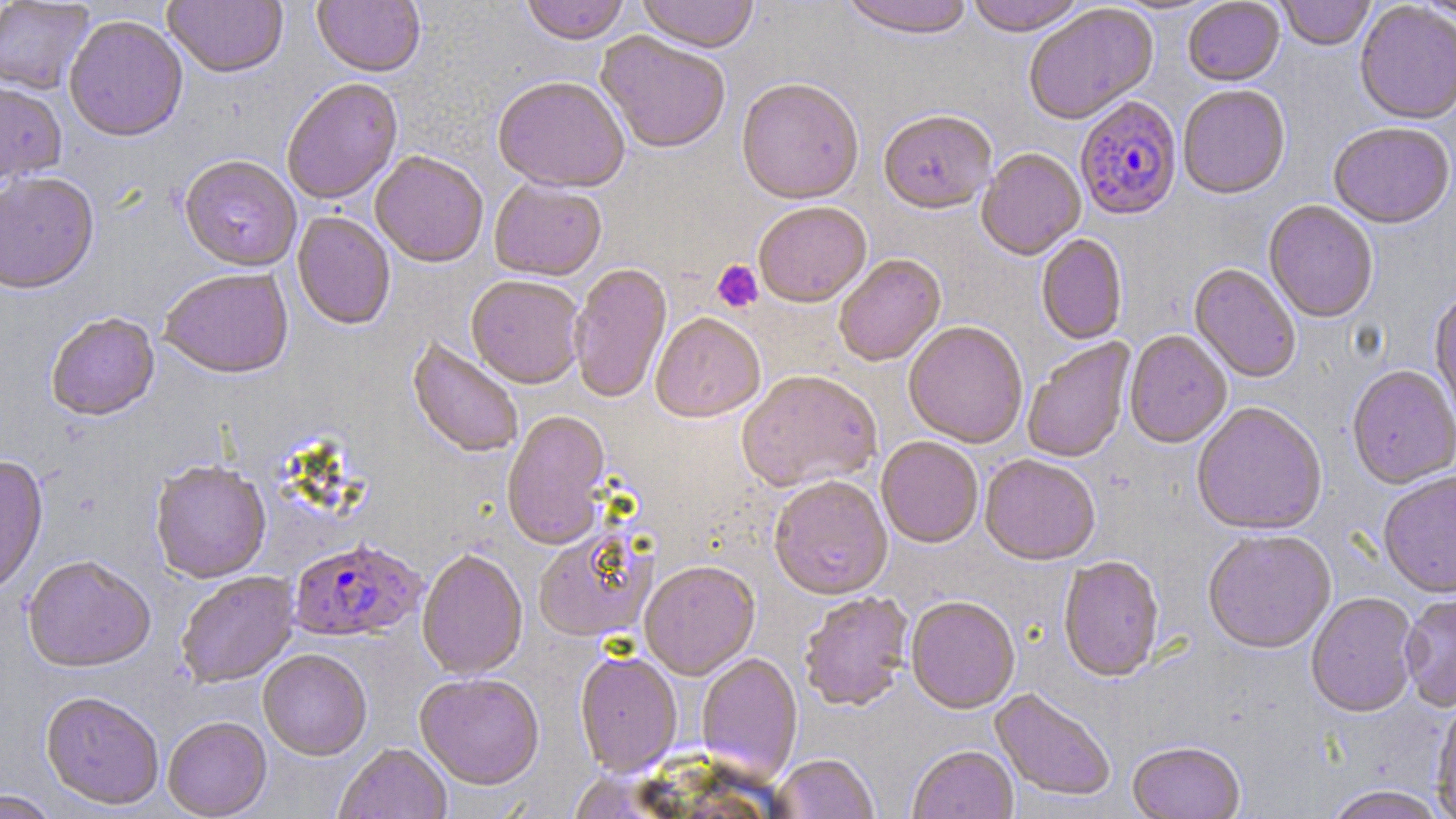
plasmodium_falciparum_infected_red_blood_cell_locations_subset: 'approximate bounding boxes as [x1, y1, x2, y2] in pixels: [1074, 97, 1182, 223]'
slide_level_diagnosis: Plasmodium falciparum
image_size: 1456×819 pixels
magnification: 1000x
preparation: thin blood smear
modality: optical microscopy
stain: May-Grünwald-Giemsa
uninfected_red_blood_cell_locations_subset: 'approximate bounding boxes as [x1, y1, x2, y2] in pixels: [520, 0, 631, 47], [636, 0, 759, 56], [840, 0, 975, 41], [965, 0, 1086, 38], [1110, 0, 1222, 15], [1275, 0, 1375, 52], [1418, 0, 1455, 24], [0, 1, 94, 95], [162, 1, 288, 79], [312, 1, 425, 79], [1183, 1, 1284, 88], [1354, 3, 1456, 126], [1024, 5, 1159, 126], [63, 15, 188, 143], [595, 33, 730, 156], [282, 78, 403, 205], [492, 79, 630, 196], [736, 80, 864, 208], [0, 82, 67, 189], [1178, 88, 1290, 201], [879, 113, 997, 217], [1328, 124, 1455, 231], [976, 150, 1086, 262], [370, 153, 488, 270], [179, 156, 302, 272], [0, 174, 99, 297], [489, 182, 607, 283], [1263, 202, 1378, 325], [754, 204, 872, 310], [292, 212, 395, 331], [1037, 236, 1128, 346], [834, 256, 946, 368], [569, 264, 673, 405], [1189, 265, 1301, 383], [158, 269, 294, 380], [466, 277, 584, 391], [1429, 289, 1456, 429], [45, 313, 160, 423], [650, 315, 765, 425], [903, 323, 1027, 450], [1124, 332, 1232, 450], [407, 339, 523, 459], [1023, 339, 1136, 464], [1347, 367, 1456, 491], [737, 372, 882, 495], [1191, 404, 1327, 538], [502, 412, 612, 550], [876, 438, 983, 550], [0, 456, 49, 599], [980, 457, 1101, 568], [151, 462, 271, 583], [1379, 474, 1456, 599], [769, 477, 893, 603], [533, 530, 656, 643], [1202, 532, 1337, 656], [417, 550, 528, 680], [22, 557, 155, 673], [1058, 558, 1165, 684], [640, 563, 761, 681], [176, 572, 299, 689], [799, 594, 914, 714], [1305, 594, 1420, 719], [1401, 595, 1456, 713], [905, 599, 1020, 716], [257, 650, 372, 761], [575, 653, 683, 778], [696, 653, 803, 784], [414, 675, 545, 791], [989, 689, 1114, 803], [41, 693, 164, 812], [1431, 701, 1456, 818], [163, 718, 272, 818], [1127, 743, 1246, 818], [335, 744, 452, 819], [908, 747, 1019, 819], [770, 756, 879, 819], [1324, 787, 1446, 819], [0, 790, 61, 818]'
field_of_view: single
platelet_locations: 'approximate bounding boxes as [x1, y1, x2, y2] in pixels: [712, 260, 763, 313]'